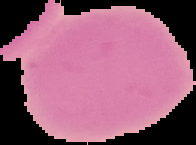
Summary:
  - Image type: segmented cell region with the area outside set to black
  - Preparation: thin blood film
  - Image size: 196×145 pixels
  - Result: no malaria parasites seen